Identify the parasite.
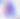
This is Toxoplasma gondii.

magnification = 400x
modality = micrograph